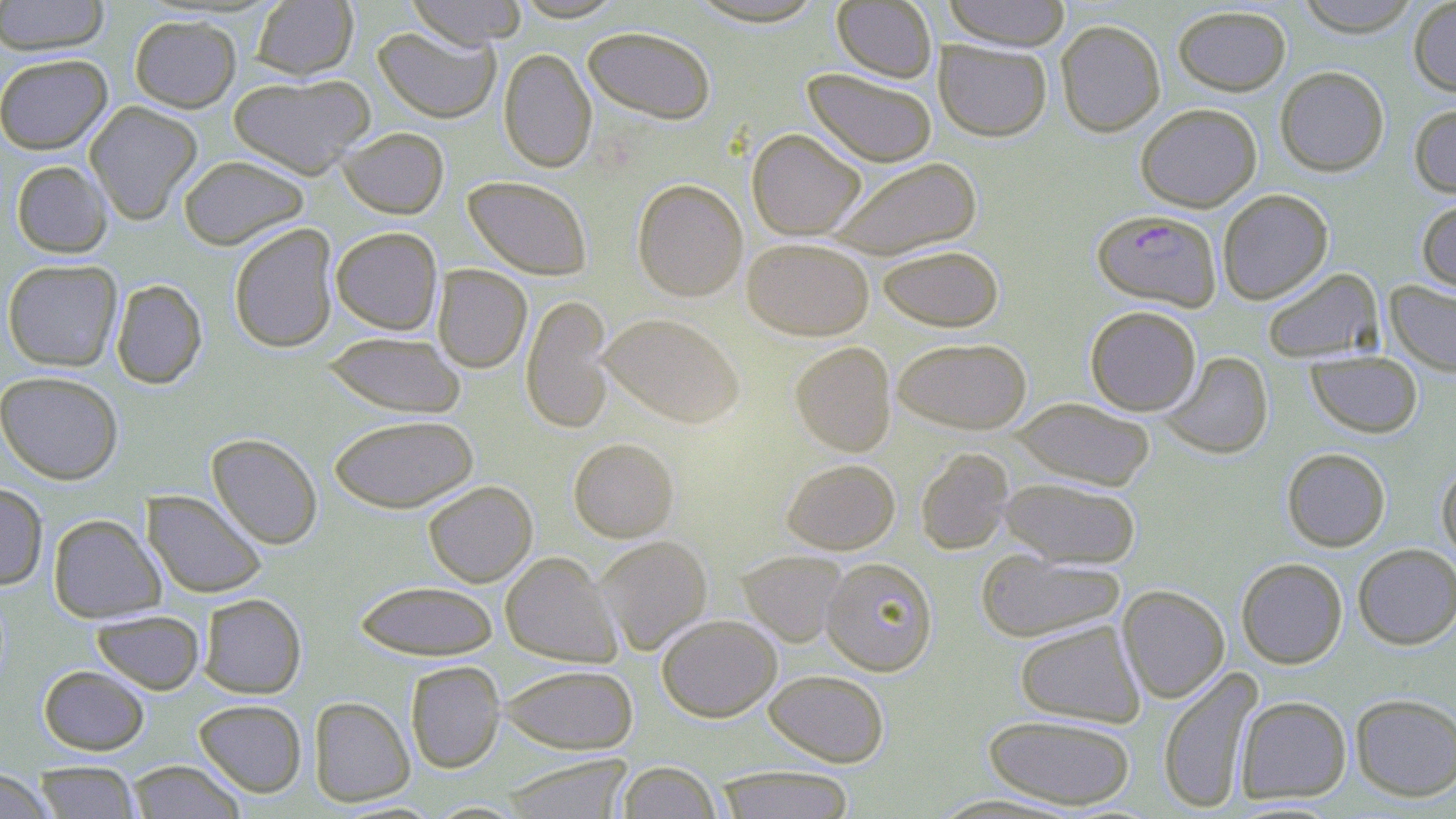

slide-level diagnosis = Plasmodium falciparum
preparation = thin blood smear
field of view = single
image size = 1456×819 pixels
modality = optical microscopy
Plasmodium falciparum-infected red blood cell locations = approximate bounding boxes as (x1, y1, x2, y2) in pixels: (1092, 209, 1222, 310)
uninfected red blood cell locations = approximate bounding boxes as (x1, y1, x2, y2) in pixels: (0, 0, 110, 56), (405, 0, 530, 47), (511, 0, 626, 21), (942, 0, 1072, 50), (1293, 0, 1423, 36), (1408, 0, 1456, 96), (251, 1, 358, 80), (684, 1, 830, 27), (832, 1, 937, 82), (1173, 5, 1291, 95), (129, 14, 241, 112), (1055, 20, 1165, 136), (373, 26, 501, 123), (582, 26, 717, 123), (934, 41, 1051, 141), (499, 48, 596, 172), (0, 53, 113, 154), (1275, 66, 1389, 176), (803, 68, 937, 167), (228, 73, 375, 178), (84, 101, 202, 224), (1409, 103, 1456, 198), (1135, 104, 1262, 212), (338, 126, 449, 219), (747, 128, 866, 239), (178, 155, 309, 249), (825, 156, 982, 259), (11, 160, 113, 258), (463, 175, 593, 279), (632, 178, 748, 301), (1217, 189, 1333, 304), (1415, 196, 1456, 293), (228, 223, 339, 353), (331, 226, 443, 334), (742, 237, 874, 340), (877, 244, 1004, 331), (2, 258, 123, 371), (432, 265, 531, 373), (1261, 267, 1383, 363), (110, 279, 207, 389), (1385, 280, 1456, 376), (521, 293, 615, 434), (1085, 305, 1201, 415), (599, 312, 746, 429), (322, 331, 467, 418), (893, 337, 1032, 433), (790, 341, 896, 456), (1159, 351, 1273, 459), (1306, 351, 1423, 437), (0, 370, 124, 484), (1011, 398, 1156, 490), (328, 414, 478, 513), (207, 433, 323, 549), (568, 438, 679, 542), (1282, 447, 1390, 551), (915, 448, 1014, 555), (781, 458, 900, 554), (1437, 462, 1456, 565), (998, 476, 1141, 568), (423, 480, 537, 587), (0, 482, 48, 589), (142, 490, 267, 599), (48, 513, 164, 623), (595, 535, 712, 655), (1353, 543, 1456, 649), (974, 549, 1126, 643), (737, 550, 849, 647), (500, 551, 621, 667), (821, 556, 938, 676), (1236, 558, 1348, 668), (355, 580, 498, 660), (1117, 585, 1230, 703), (198, 593, 306, 698), (91, 609, 205, 694), (657, 614, 782, 721), (1014, 620, 1145, 727), (406, 661, 505, 773), (500, 663, 639, 754), (38, 665, 150, 755), (1158, 666, 1263, 815), (763, 669, 889, 767), (1350, 693, 1456, 801), (1236, 695, 1352, 803), (308, 696, 415, 807), (193, 698, 307, 797), (983, 714, 1136, 809), (500, 755, 634, 819), (126, 760, 246, 818), (32, 761, 141, 818), (615, 761, 722, 819), (714, 765, 856, 818), (0, 768, 55, 819)
stain = May-Grünwald-Giemsa
magnification = 1000x